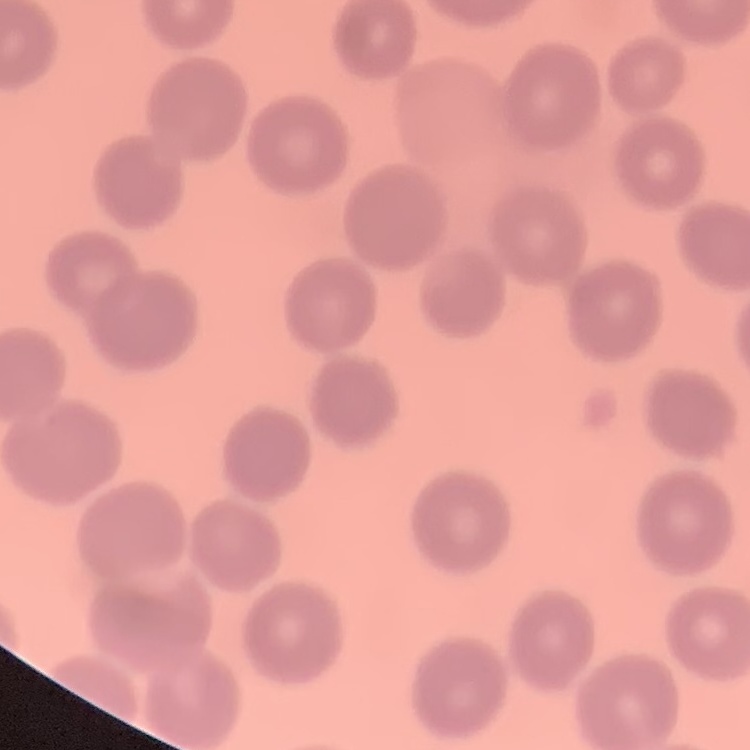

Summary:
  - Red blood cell morphology: no rouleaux formation
  - Image type: square crop of a larger photomicrograph
  - Stain: Field's or Giemsa
  - Preparation: thin blood film